Evaluate for malaria.
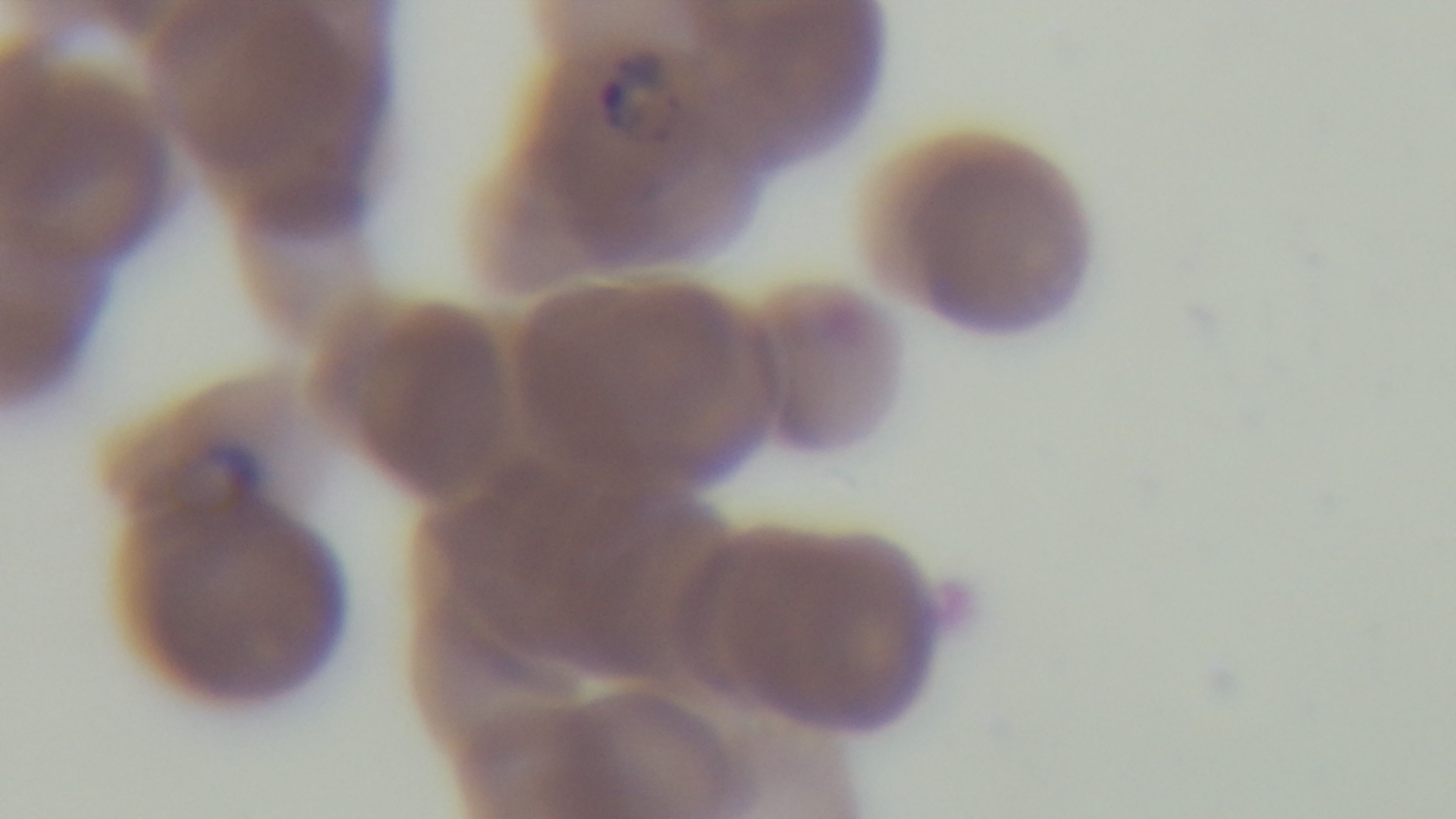
Infected.

Oil-immersion objective, 100x. Light microscopy. Preparation: thin. Mounted 4K digital camera. Giemsa-stained. Single field of view.